Draw a bounding box around every malaria parasite, every leukocyte, and every artifact (stain precipitate or debris).
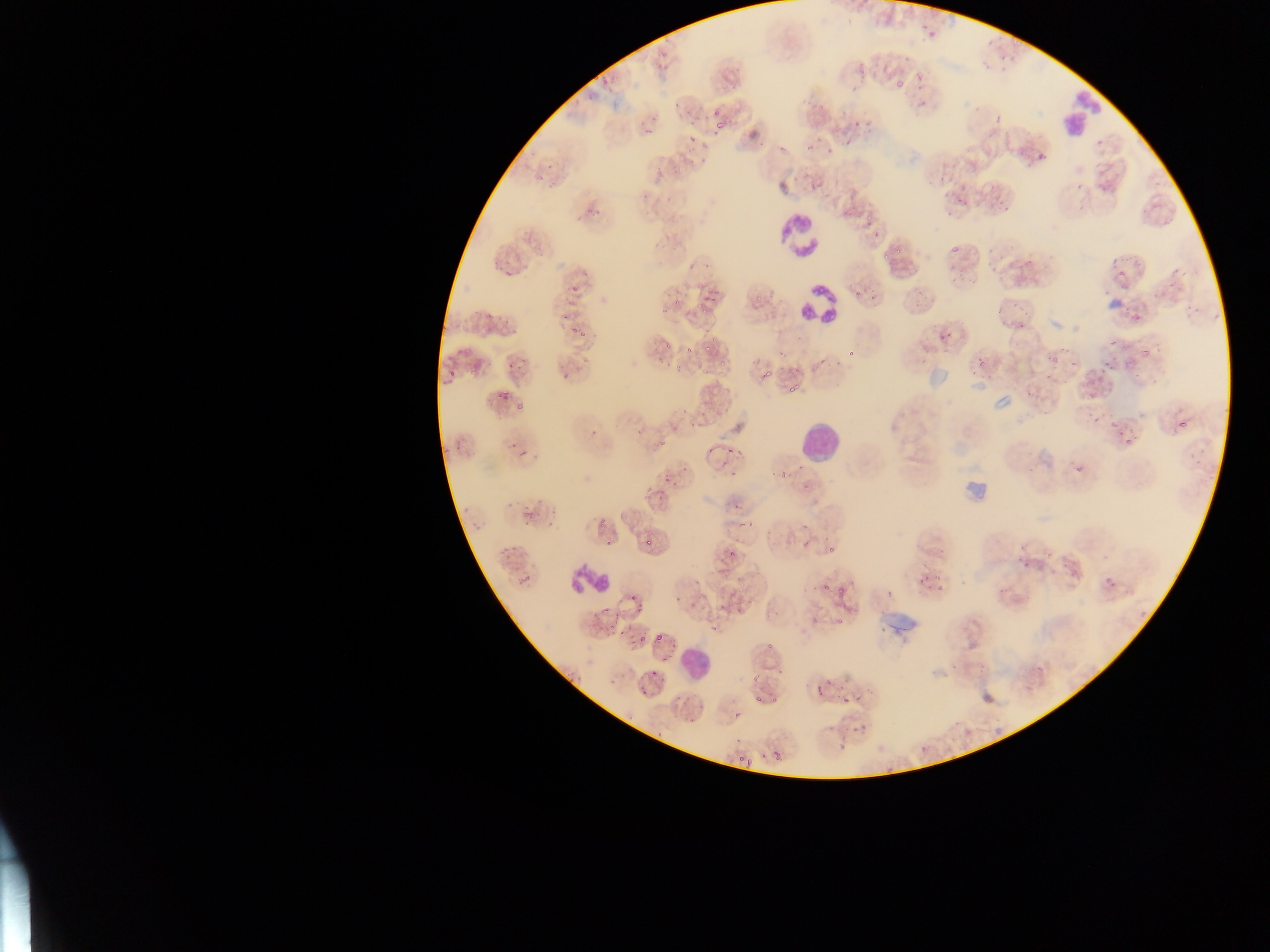

Approximate bounding boxes as (left, top, right, bottom) in pixels.
Malaria parasites: (699, 156, 707, 164), (593, 208, 601, 216), (871, 222, 885, 238), (893, 243, 904, 257), (946, 245, 959, 256), (1128, 255, 1139, 264), (1114, 264, 1130, 280), (854, 285, 865, 296), (704, 287, 715, 296), (569, 288, 578, 294), (751, 293, 762, 306), (672, 298, 682, 309), (696, 303, 710, 313), (1131, 307, 1154, 325), (1012, 317, 1026, 331), (576, 329, 587, 338), (1044, 340, 1062, 369), (1108, 341, 1121, 363), (682, 343, 696, 356), (848, 346, 857, 358), (700, 347, 708, 355), (1138, 347, 1151, 358), (971, 356, 989, 370), (1101, 356, 1121, 373), (722, 362, 729, 370), (447, 366, 459, 382), (761, 366, 776, 382), (701, 369, 709, 378), (561, 374, 569, 382), (787, 386, 798, 400), (498, 392, 506, 405), (514, 400, 525, 413), (1092, 417, 1100, 426), (1108, 417, 1122, 432), (1177, 418, 1188, 429), (590, 430, 598, 438), (1124, 432, 1138, 446), (734, 443, 745, 455), (1075, 465, 1084, 474), (780, 471, 789, 478), (659, 473, 666, 486), (667, 477, 685, 489), (523, 504, 539, 521), (744, 514, 761, 528), (606, 540, 612, 548), (643, 540, 651, 549), (823, 544, 836, 556), (726, 549, 734, 558), (1018, 560, 1030, 571), (1104, 573, 1118, 591), (823, 580, 832, 591), (937, 587, 946, 599), (841, 588, 850, 592), (628, 595, 638, 607), (736, 608, 747, 619), (834, 620, 843, 631), (637, 631, 648, 646), (656, 633, 666, 644), (766, 644, 776, 650), (751, 668, 763, 685), (819, 680, 829, 692), (640, 689, 647, 697), (842, 696, 851, 704), (753, 697, 761, 703), (771, 697, 778, 707), (772, 751, 779, 759) | approximate (x, y) pixel centers of objects too small to bound: (922, 104), (572, 332), (603, 522), (1048, 557), (604, 611), (653, 673), (629, 717).
Leukocytes: (1050, 98, 1103, 156), (777, 212, 823, 259), (800, 285, 837, 323), (801, 422, 837, 456), (568, 564, 612, 595), (681, 647, 707, 677).

Summary:
  - Country: Ghana
  - Capture: mobile-phone photograph through a microscope
  - Preparation: thin blood smear
  - Field of view: single
  - Image size: 1270×952 pixels